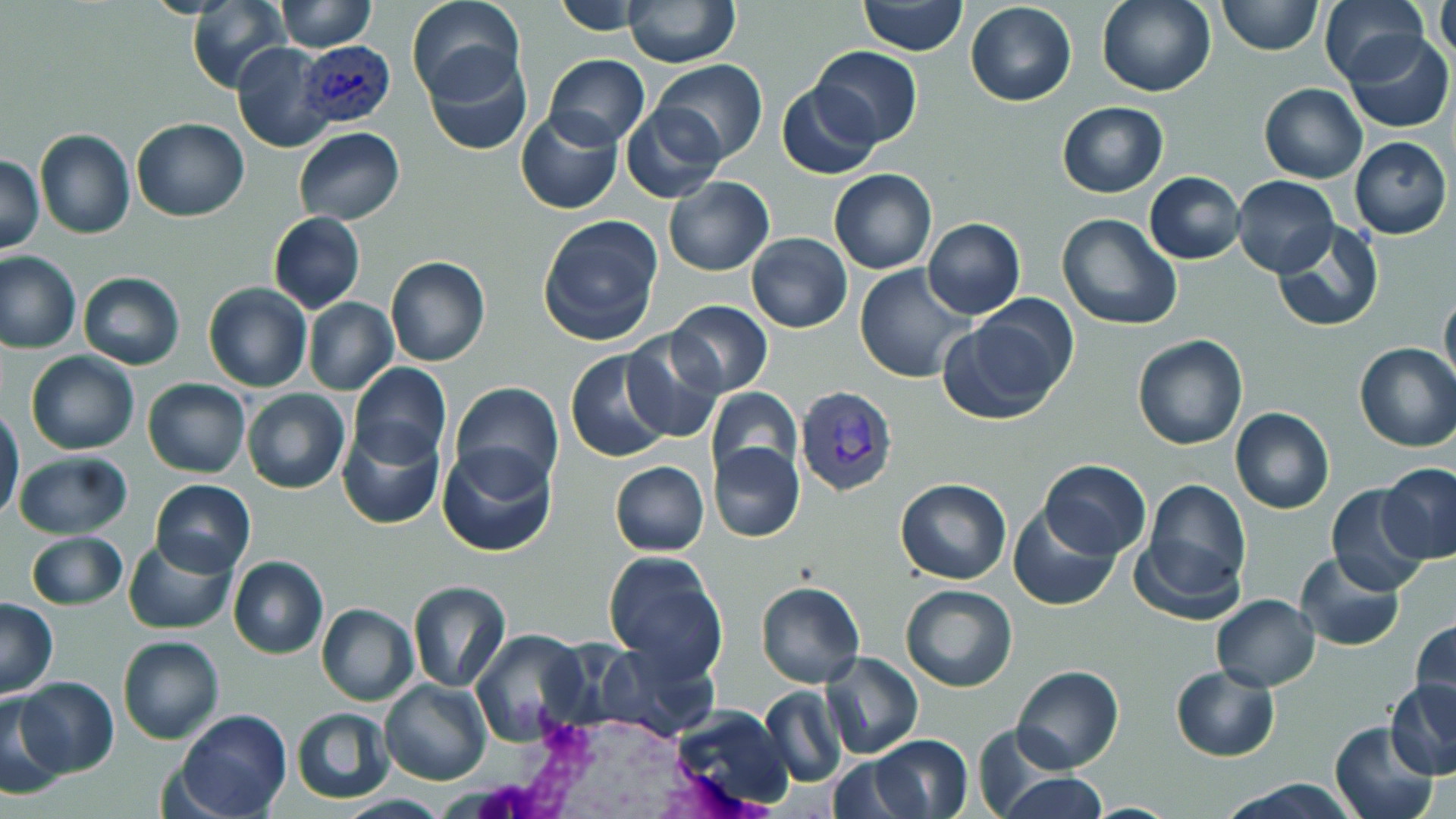

{
  "slide_level_diagnosis": "Plasmodium vivax",
  "stain": "May-Grünwald-Giemsa",
  "preparation": "thin blood film",
  "modality": "optical microscopy",
  "white_blood_cell_locations": "approximate bounding boxes as [x1, y1, x2, y2] in pixels: [471, 707, 780, 819]",
  "magnification": "1000x",
  "field_of_view": "single",
  "plasmodium_vivax_infected_red_blood_cell_locations": "approximate bounding boxes as [x1, y1, x2, y2] in pixels: [298, 39, 395, 127], [793, 385, 898, 495]",
  "image_size": "1456×819 pixels",
  "uninfected_red_blood_cell_locations": "approximate bounding boxes as [x1, y1, x2, y2] in pixels: [406, 0, 523, 104], [553, 0, 650, 34], [622, 0, 739, 67], [1098, 0, 1217, 97], [1218, 0, 1322, 55], [1319, 0, 1430, 86], [1433, 0, 1455, 70], [186, 1, 289, 92], [277, 1, 376, 52], [860, 1, 968, 55], [967, 2, 1076, 106], [1345, 31, 1453, 131], [232, 40, 337, 154], [422, 47, 533, 155], [811, 47, 923, 146], [543, 55, 649, 148], [651, 60, 767, 163], [776, 82, 881, 180], [1259, 83, 1367, 183], [1056, 101, 1169, 198], [621, 104, 729, 201], [515, 109, 624, 214], [131, 118, 250, 220], [293, 127, 404, 225], [34, 130, 135, 240], [1349, 138, 1452, 239], [0, 155, 44, 253], [829, 170, 937, 275], [1144, 172, 1245, 265], [662, 175, 774, 275], [1231, 175, 1340, 277], [267, 211, 365, 313], [1056, 213, 1183, 331], [537, 216, 663, 346], [922, 218, 1026, 321], [1271, 220, 1384, 333], [747, 233, 851, 332], [0, 252, 81, 354], [386, 257, 490, 367], [856, 265, 976, 384], [78, 272, 184, 369], [202, 283, 312, 393], [1440, 288, 1456, 392], [303, 297, 398, 396], [666, 299, 773, 398], [943, 308, 1075, 425], [619, 330, 727, 443], [1133, 334, 1249, 451], [1354, 342, 1456, 452], [566, 349, 674, 464], [26, 351, 138, 454], [350, 361, 452, 469], [142, 378, 250, 479], [448, 382, 563, 493], [703, 386, 802, 486], [242, 388, 350, 495], [1230, 407, 1334, 514], [0, 408, 25, 523], [337, 422, 445, 531], [710, 442, 805, 542], [435, 444, 559, 558], [14, 451, 132, 539], [1040, 459, 1151, 559], [608, 461, 709, 556], [1379, 464, 1455, 564], [150, 478, 255, 576], [894, 478, 1012, 584], [1140, 479, 1251, 599], [1325, 485, 1433, 596], [1008, 507, 1121, 611], [26, 530, 127, 610], [1131, 531, 1245, 627], [122, 537, 236, 634], [602, 551, 727, 675], [1295, 552, 1404, 651], [227, 555, 328, 658], [755, 580, 865, 688], [406, 581, 511, 692], [900, 583, 1017, 692], [1211, 594, 1321, 690], [0, 598, 58, 698], [316, 603, 418, 705], [1411, 616, 1456, 722], [471, 630, 590, 747], [117, 635, 223, 744], [589, 638, 720, 741], [822, 651, 923, 760], [1012, 665, 1123, 772], [1170, 665, 1280, 760], [13, 677, 119, 778], [1386, 678, 1456, 780], [379, 679, 491, 786], [760, 686, 846, 788], [0, 695, 67, 800], [667, 706, 795, 813], [290, 707, 394, 804], [173, 710, 291, 819], [1330, 721, 1440, 819], [968, 727, 1072, 818], [869, 735, 975, 819], [826, 757, 922, 818], [994, 773, 1109, 818], [1215, 778, 1359, 818], [331, 793, 455, 819]"
}